State which parasite is depicted.
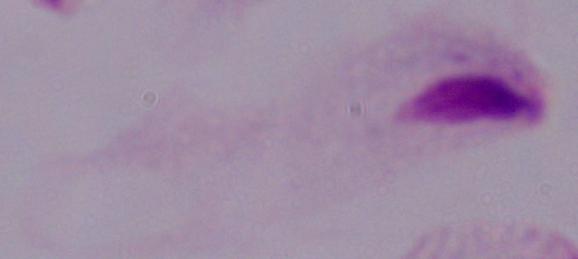

A trichomonad.

magnification = 1000x
modality = photomicrograph